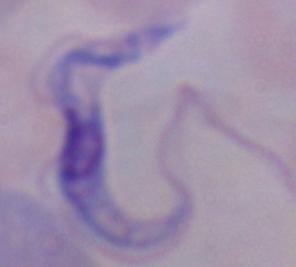 Captured at 1000x magnification. Photomicrograph. A trypanosome is seen.